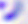
Summary:
  - Identification: Toxoplasma gondii
  - Modality: photomicrograph
  - Magnification: 400x